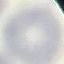
Summary:
  - Malaria status: uninfected
  - Capture: smartphone camera at the microscope eyepiece
  - Image type: automatically extracted cell patch, resized to 64 × 64 pixels
  - Preparation: thin blood film
  - Stain: Giemsa